Report the malaria status of this cell.
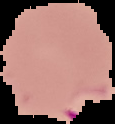

It is parasitized.

From a thin blood smear. Image is 115×124 pixels. The area outside the segmented cell region is set to black.